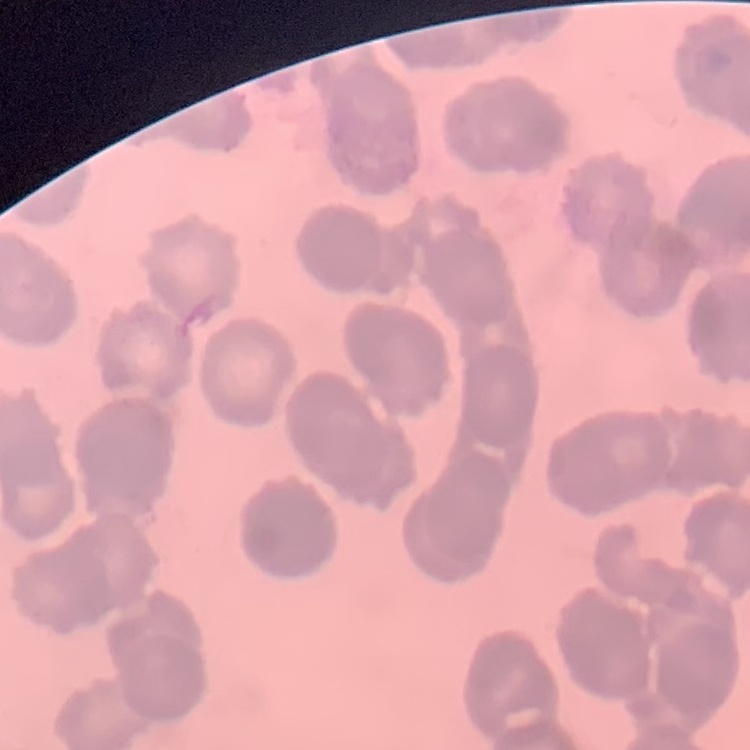

The erythrocytes exhibit rouleaux formation. Square crop of a larger photomicrograph. Field's or Giemsa stain. Thin blood film.